Classify this cell by malaria status.
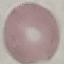
Uninfected.

preparation: thin blood smear
capture: smartphone camera at the microscope eyepiece
stain: Giemsa
image_type: automatically extracted cell patch, resized to 64 × 64 pixels